Assess for malaria.
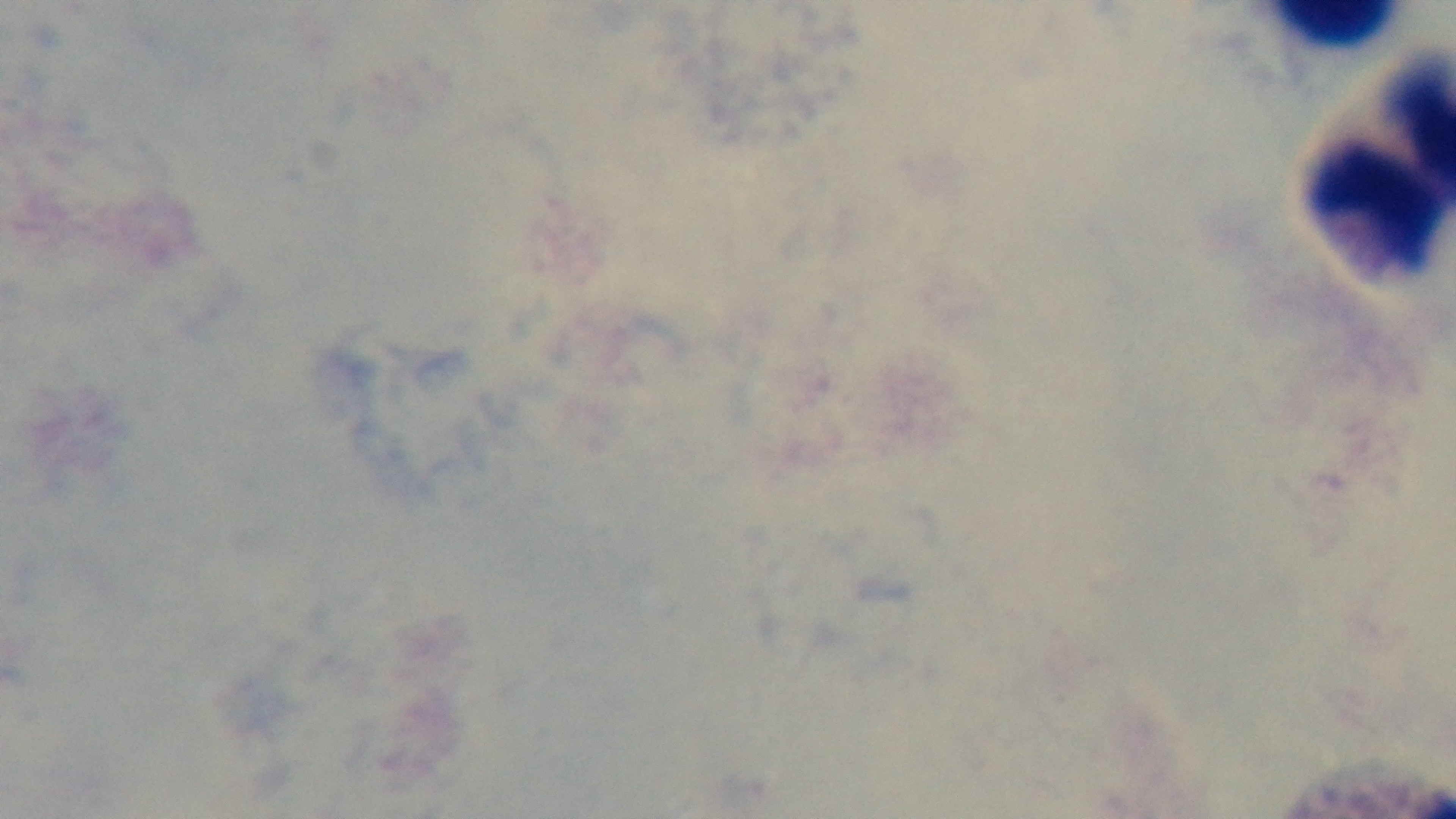
It is uninfected.

Photomicrograph. Oil-immersion objective, 100x. Preparation: thick smear. One field from the slide. Giemsa-stained. Mounted 4K digital camera.